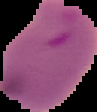
Summary:
  - Preparation: thin blood film
  - Image size: 97×112 pixels
  - Image type: segmented cell region on a black background
  - Malaria status: parasitized